Assess this cell for malaria.
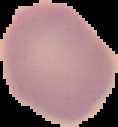

Uninfected.

Image is 118×127 pixels. From a thin blood smear. Segmented cell region on a black background.